Name the cell type shown.
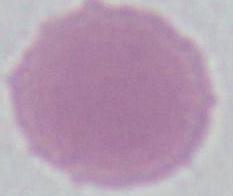

An erythrocyte.

Photomicrograph. 1000x magnification.